Outline each blood parasite and name the species.
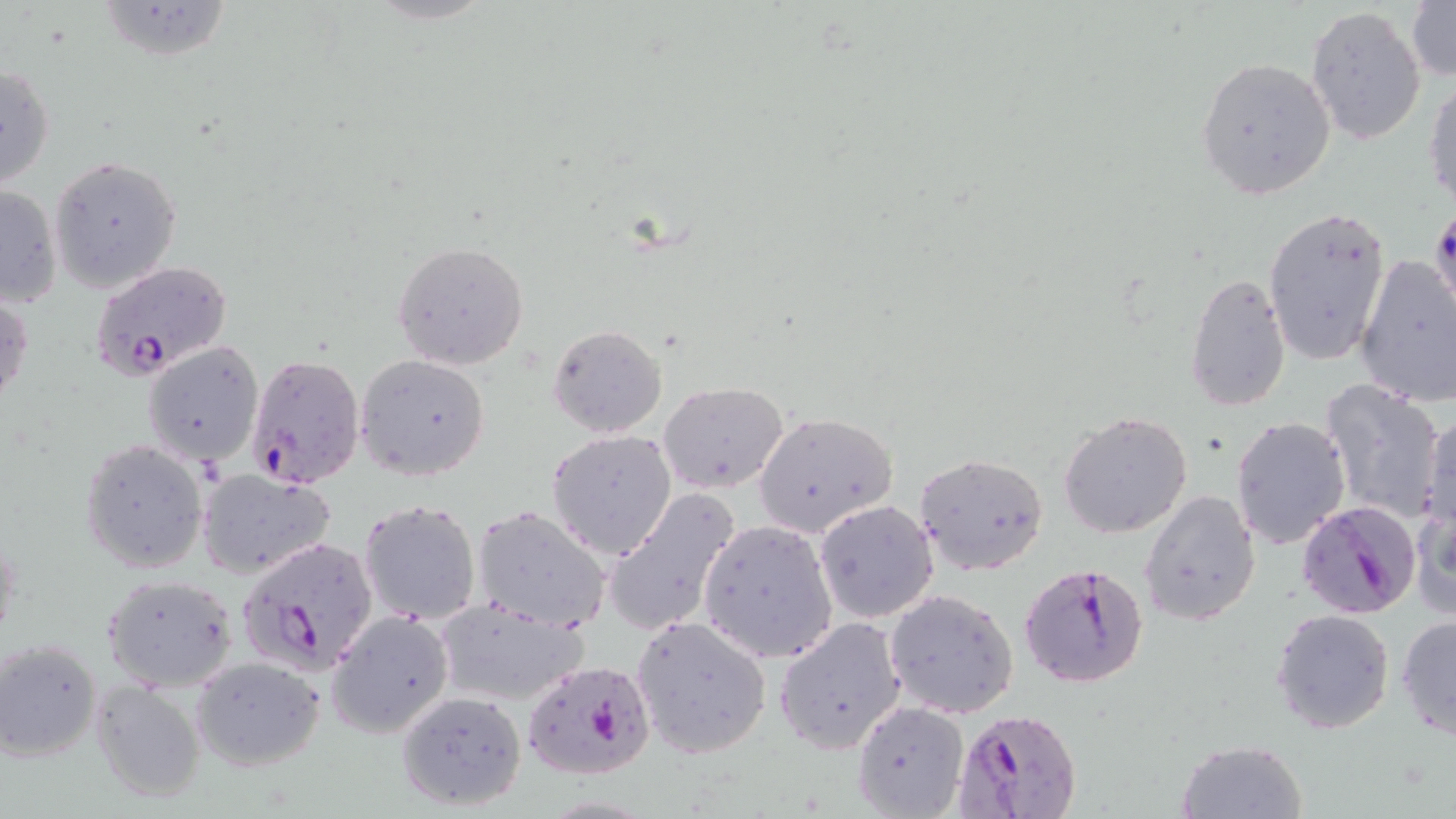
Approximate bounding boxes as [x1, y1, x2, y2] in pixels.
Plasmodium falciparum-infected red blood cells: [90, 260, 234, 381], [247, 353, 365, 488], [1295, 500, 1421, 617], [237, 533, 380, 676], [1021, 561, 1148, 687], [520, 660, 654, 781], [949, 708, 1084, 819].
No Plasmodium ovale, Plasmodium malariae, Plasmodium vivax, Babesia divergens, or Trypanosoma brucei observed.

Summary:
  - Uninfected red blood cell locations: [95, 0, 235, 62], [1406, 0, 1455, 82], [1305, 7, 1426, 145], [1195, 56, 1336, 201], [0, 61, 55, 193], [1425, 78, 1456, 211], [49, 156, 182, 292], [0, 182, 63, 309], [1429, 205, 1456, 316], [1263, 206, 1392, 366], [392, 241, 530, 371], [1355, 256, 1456, 407], [1183, 271, 1291, 413], [0, 288, 32, 413], [547, 323, 668, 439], [144, 342, 265, 466], [355, 354, 491, 481], [1317, 381, 1447, 525], [659, 382, 788, 494], [1058, 411, 1192, 539], [753, 412, 898, 536], [1421, 413, 1456, 539], [1232, 417, 1351, 549], [547, 430, 677, 558], [80, 438, 208, 573], [915, 453, 1050, 576], [197, 468, 336, 579], [601, 486, 743, 639], [1140, 490, 1261, 626], [1412, 496, 1455, 626], [360, 500, 480, 625], [815, 500, 939, 623], [471, 506, 612, 631], [697, 520, 837, 663], [102, 574, 239, 691], [886, 587, 1019, 719], [432, 597, 590, 709], [1271, 608, 1396, 735], [327, 611, 453, 739], [1397, 614, 1456, 741], [631, 615, 772, 758], [775, 618, 907, 752], [0, 638, 104, 763], [190, 656, 322, 771], [90, 679, 208, 803], [395, 689, 527, 810], [851, 701, 969, 817], [1175, 739, 1309, 819]
  - Slide-level diagnosis: Plasmodium falciparum
  - Image size: 1456×819 pixels
  - Stain: May-Grünwald-Giemsa
  - Field of view: single
  - Modality: light microscopy
  - Preparation: thin blood smear
  - Magnification: 1000x